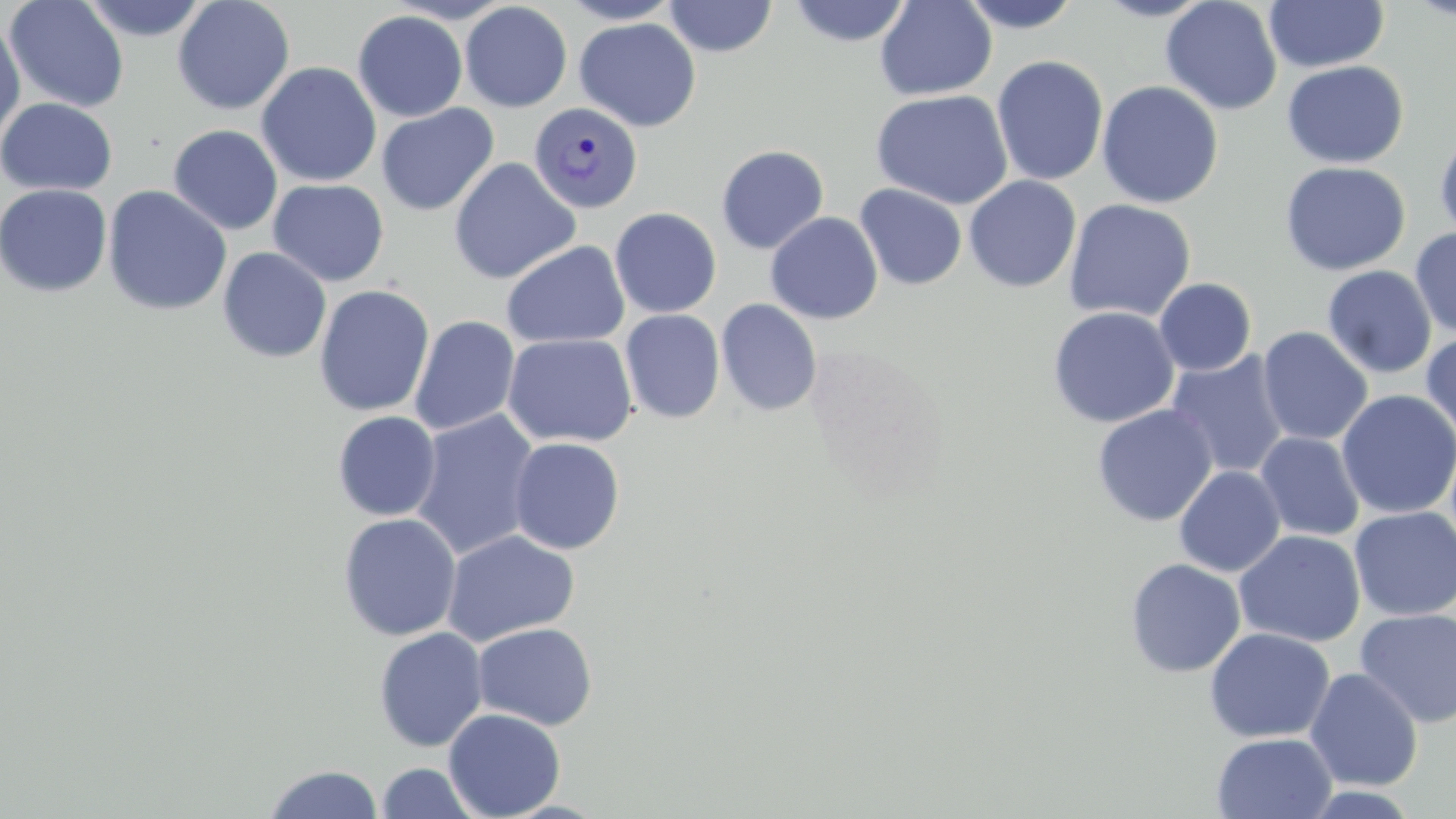

slide_level_diagnosis: Plasmodium vivax
field_of_view: single
magnification: 1000x
uninfected_red_blood_cell_locations: 'approximate bounding boxes as (x1, y1, x2, y2) in pixels: (4, 0, 130, 113), (80, 0, 210, 42), (172, 0, 295, 115), (559, 0, 683, 24), (663, 0, 778, 58), (788, 0, 913, 47), (874, 0, 997, 101), (958, 0, 1083, 33), (1093, 0, 1217, 22), (1160, 0, 1283, 116), (1264, 1, 1389, 72), (460, 2, 573, 112), (352, 10, 467, 122), (0, 16, 26, 148), (574, 17, 700, 133), (991, 55, 1109, 186), (1282, 60, 1409, 169), (256, 61, 381, 187), (1096, 80, 1224, 208), (871, 88, 1013, 210), (0, 98, 118, 196), (376, 103, 499, 216), (168, 124, 283, 235), (1434, 131, 1456, 243), (716, 145, 829, 254), (449, 158, 580, 284), (1280, 161, 1411, 276), (964, 175, 1081, 293), (267, 178, 389, 287), (0, 183, 113, 298), (102, 184, 233, 317), (854, 184, 967, 290), (1063, 198, 1196, 322), (610, 207, 722, 319), (765, 212, 883, 325), (1410, 228, 1456, 338), (501, 240, 629, 349), (217, 247, 332, 363), (1322, 265, 1437, 379), (1154, 278, 1257, 376), (313, 285, 435, 417), (716, 299, 822, 416), (1047, 306, 1180, 428), (620, 309, 725, 424), (409, 315, 520, 436), (1257, 326, 1373, 446), (1421, 331, 1456, 445), (502, 333, 638, 448), (1166, 351, 1290, 478), (1336, 389, 1456, 520), (1092, 404, 1218, 526), (410, 409, 541, 561), (332, 411, 441, 521), (1254, 432, 1365, 542), (508, 437, 626, 555), (1174, 465, 1285, 577), (1349, 506, 1456, 621), (338, 513, 461, 641), (441, 529, 580, 647), (1234, 530, 1365, 647), (1124, 558, 1246, 679), (1354, 608, 1456, 727), (473, 623, 598, 730), (373, 626, 488, 752), (1204, 627, 1335, 743), (1304, 668, 1423, 792), (443, 708, 567, 819), (1211, 732, 1337, 819), (375, 762, 482, 818), (263, 764, 384, 819)'
preparation: thin blood film
image_size: 1456×819 pixels
plasmodium_vivax_infected_red_blood_cell_locations: 'approximate bounding boxes as (x1, y1, x2, y2) in pixels: (529, 103, 643, 213)'
stain: May-Grünwald-Giemsa
modality: light microscopy